Describe the morphology of the red blood cells.
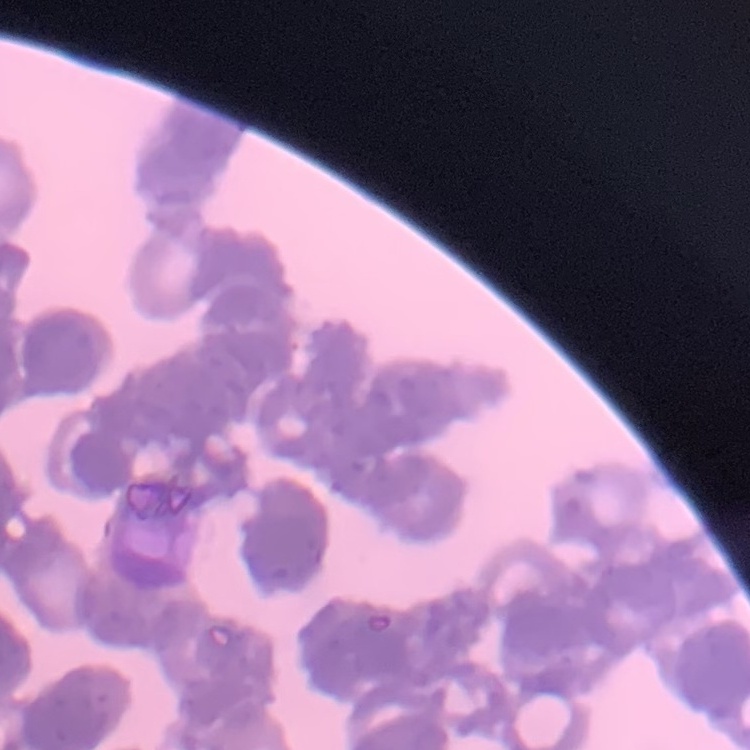

They show rouleaux formation.

preparation = thin blood smear
stain = Field's or Giemsa
image type = square crop of a larger photomicrograph